Give the extent of all Plasmodium falciparum-infected red blood cells.
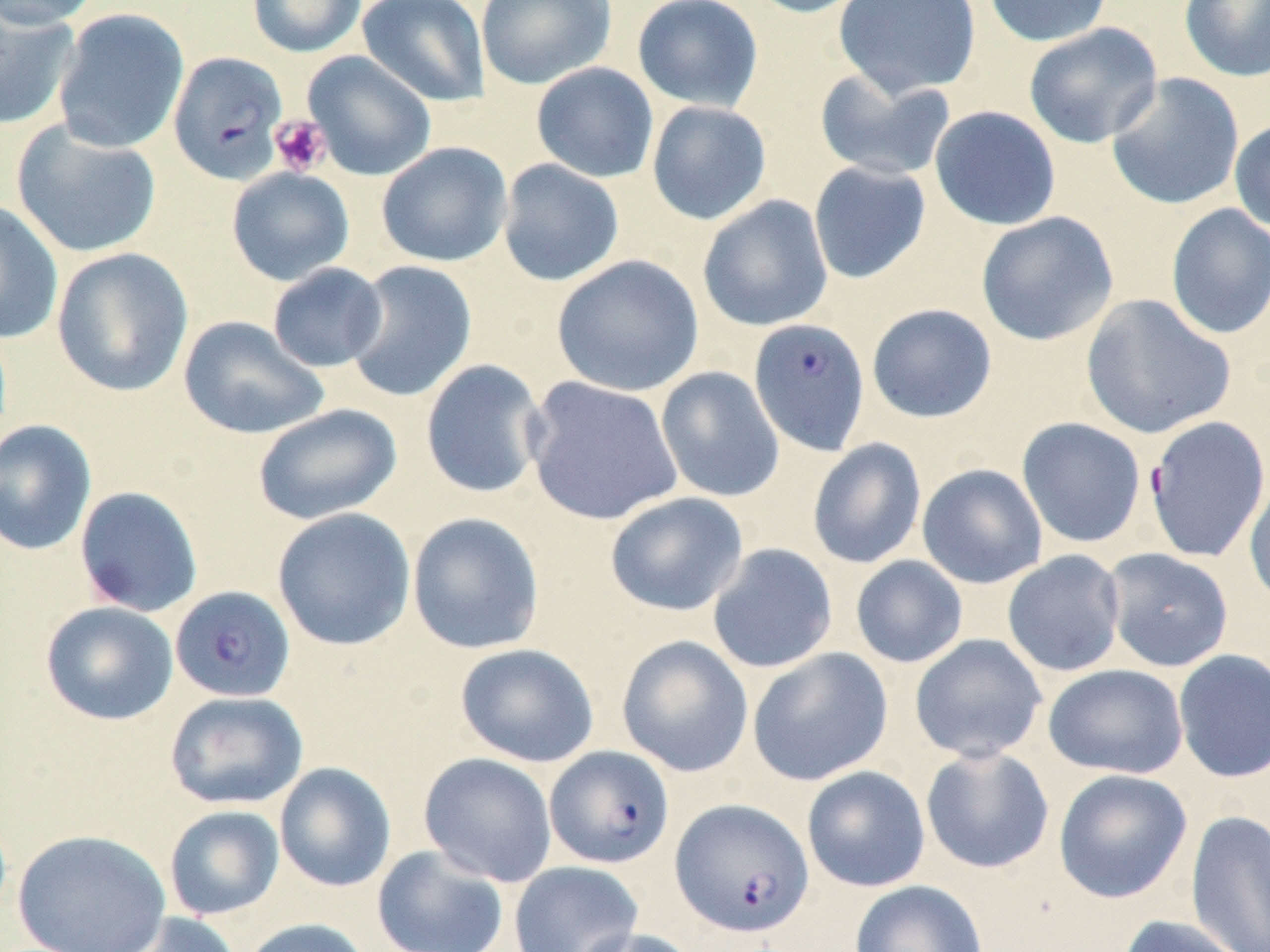
Approximate bounding boxes as (x1,y1)-(x2,y2) corner pairs in pixels.
Plasmodium falciparum-infected red blood cells: (168,51)-(289,185), (748,318)-(870,455), (1144,415)-(1270,563), (170,585)-(295,703), (544,745)-(676,869), (669,798)-(814,938).

Platelet locations: (269,114)-(332,176). Uninfected red blood cell locations: (0,0)-(103,29), (247,0)-(367,57), (357,0)-(490,107), (475,0)-(616,89), (632,0)-(764,112), (742,0)-(873,18), (833,0)-(982,99), (982,0)-(1114,47), (1179,0)-(1270,82), (0,3)-(80,131), (52,8)-(190,154), (1023,22)-(1163,149), (302,51)-(436,181), (530,62)-(659,183), (813,68)-(956,182), (1106,72)-(1245,211), (646,100)-(772,224), (929,105)-(1061,231), (1228,118)-(1270,233), (10,120)-(162,259), (376,141)-(513,267), (497,159)-(625,287), (808,161)-(931,284), (225,166)-(355,286), (697,195)-(834,332), (0,200)-(63,344), (1165,203)-(1270,340), (975,211)-(1119,346), (50,247)-(194,397), (551,255)-(704,397), (343,260)-(477,403), (267,262)-(388,373), (1080,293)-(1236,440), (866,303)-(997,423), (178,315)-(328,440), (420,359)-(548,500), (655,366)-(785,502), (524,376)-(684,526), (252,403)-(403,525), (1017,417)-(1146,548), (0,419)-(97,556), (807,437)-(927,569), (917,463)-(1048,589), (1244,477)-(1270,608), (74,485)-(204,618), (604,491)-(748,617), (272,508)-(416,651), (407,512)-(545,655), (706,543)-(838,674), (1102,547)-(1234,672), (1002,549)-(1126,677), (850,555)-(969,668), (39,601)-(178,726), (615,634)-(754,778), (909,634)-(1048,763), (455,643)-(600,768), (747,647)-(893,786), (1172,648)-(1270,784), (1043,664)-(1189,778), (164,690)-(309,810), (920,745)-(1055,874), (418,752)-(558,887), (273,762)-(397,892), (801,765)-(930,892), (1052,769)-(1193,903), (163,805)-(285,920), (1186,808)-(1270,952), (12,828)-(172,952), (372,845)-(510,952), (508,861)-(643,952), (849,880)-(988,952), (103,912)-(244,952), (1116,914)-(1250,952), (241,918)-(373,952), (569,927)-(700,952). Slide-level diagnosis: Plasmodium falciparum. Thin blood film. May-Grünwald-Giemsa-stained preparation. 1000x magnification. Image is 1270×952 pixels. Single field of view. Light microscopy.